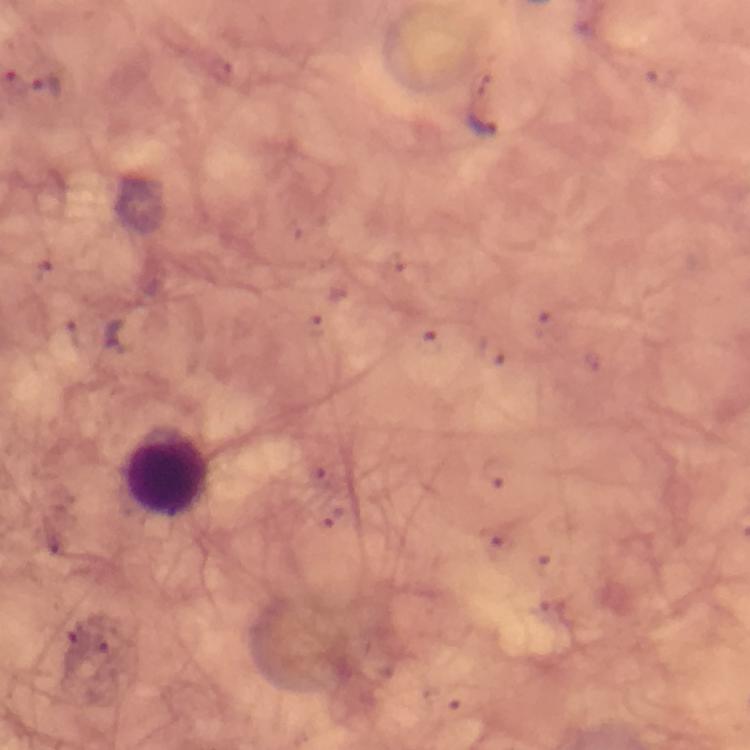

malaria parasite locations = approximate object centers, in pixels from the top-left corner: (x=46, y=88), (x=481, y=126), (x=123, y=339)
magnification = 100x
stain = Giemsa
preparation = thick blood film
context = from a diagnostic examination for malaria
immersion oil = applied
leukocyte locations = approximate object centers, in pixels from the top-left corner: (x=167, y=471)
capture = smartphone mounted on the microscope
image size = 750×750 pixels
cropped from = one field of view